Point out each Plasmodium parasite.
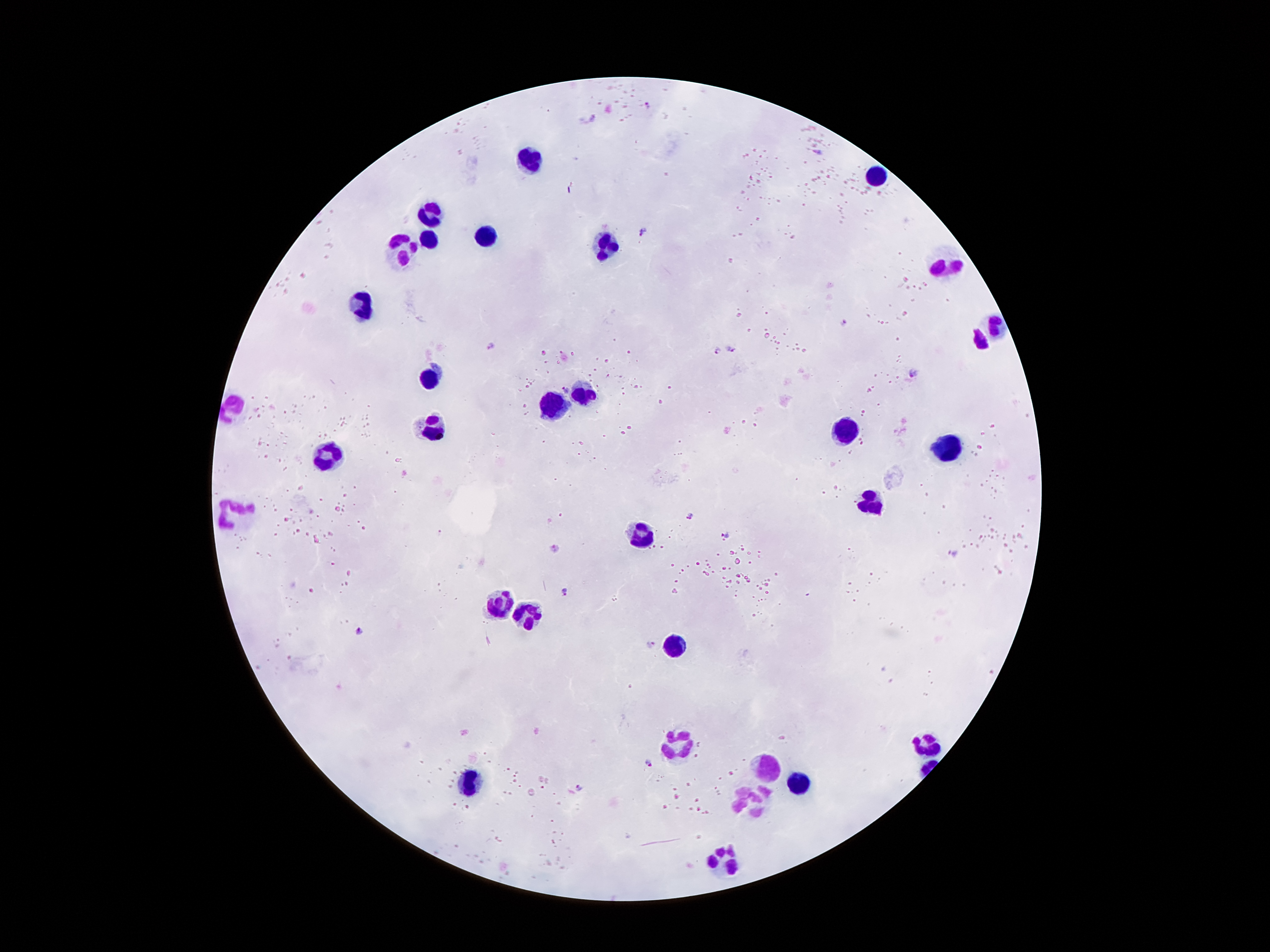

Approximate object centers, in pixels from the top-left corner.
Plasmodium parasites: (x=648, y=104), (x=594, y=118), (x=817, y=150), (x=644, y=233), (x=842, y=323), (x=491, y=345), (x=732, y=350), (x=715, y=351), (x=914, y=374), (x=567, y=390), (x=689, y=515), (x=441, y=531), (x=724, y=535), (x=555, y=548), (x=952, y=553), (x=565, y=591), (x=358, y=631), (x=653, y=643), (x=650, y=763), (x=579, y=787).

Leukocyte locations: (x=535, y=157), (x=877, y=176), (x=434, y=216), (x=485, y=231), (x=428, y=239), (x=607, y=242), (x=403, y=246), (x=947, y=265), (x=359, y=300), (x=997, y=330), (x=980, y=342), (x=434, y=376), (x=590, y=395), (x=554, y=405), (x=235, y=407), (x=435, y=428), (x=850, y=428), (x=942, y=447), (x=330, y=456), (x=869, y=502), (x=231, y=510), (x=646, y=533), (x=502, y=599), (x=533, y=615), (x=674, y=647), (x=678, y=741), (x=928, y=744), (x=768, y=767), (x=470, y=781), (x=798, y=783), (x=751, y=798), (x=724, y=863). Image is 1270×952 pixels. One field from this slide. Patient malaria status: positive for Plasmodium falciparum. 100x magnification. Smartphone photograph taken through the microscope eyepiece. Thick peripheral-blood smear. Giemsa stain.